Report the malaria status of this cell.
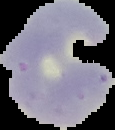

It is parasitized.

Summary:
  - Image type: segmented cell region on a black background
  - Preparation: thin blood film
  - Image size: 115×130 pixels